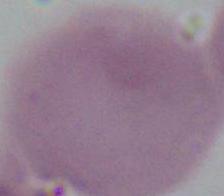
identification = red blood cell
modality = photomicrograph
magnification = 1000x